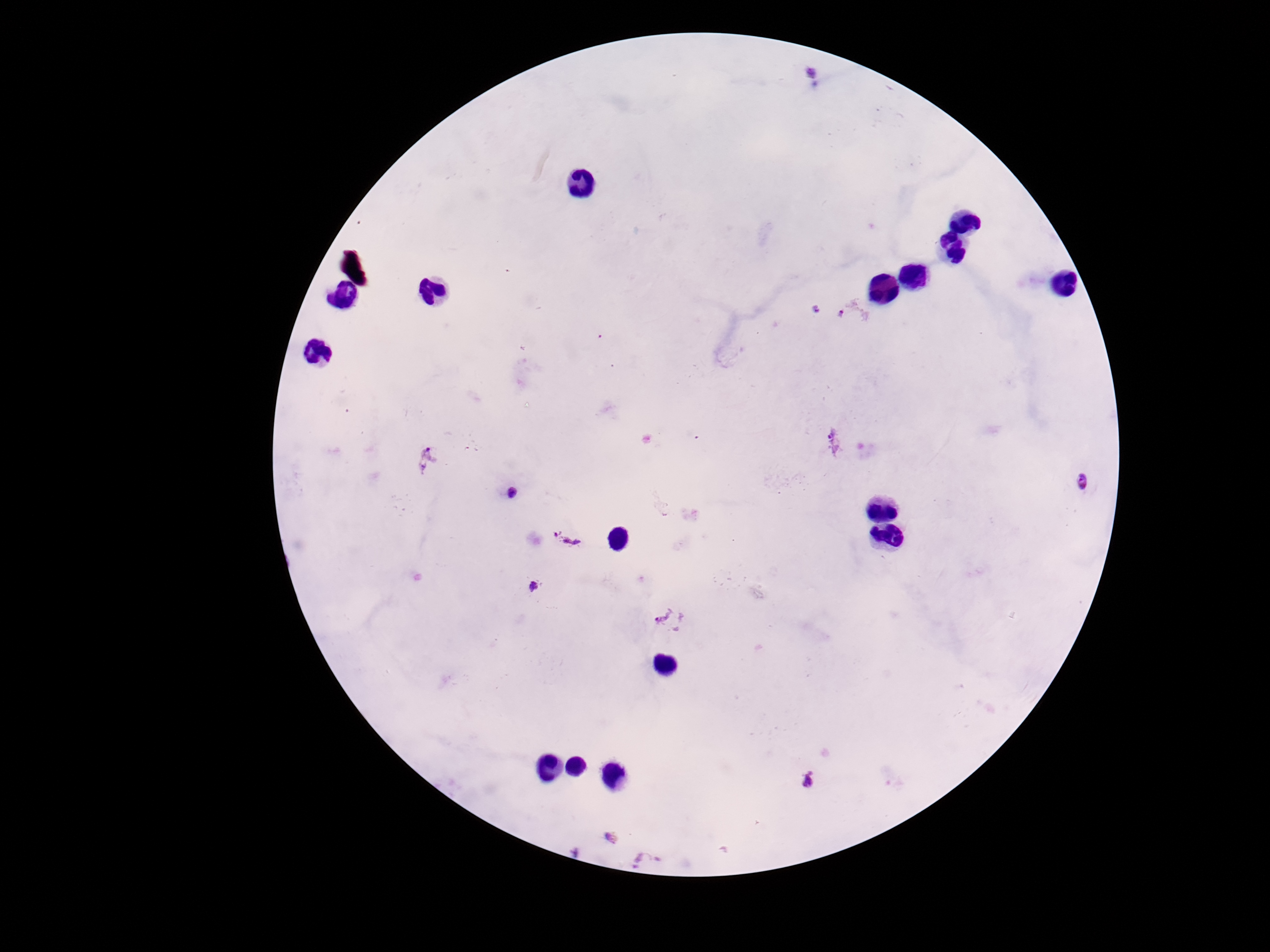
Approximate object centers, in pixels from the top-left corner. Plasmodium parasite locations: (x=814, y=76), (x=816, y=309), (x=854, y=312), (x=834, y=441), (x=428, y=459), (x=1085, y=481), (x=513, y=492), (x=561, y=539), (x=535, y=588), (x=673, y=621), (x=808, y=779), (x=609, y=837), (x=649, y=861). Image is 1270×952 pixels. 100x magnification. Smartphone photograph taken through the microscope eyepiece. Thick blood film. Patient malaria status: positive. Giemsa stain. One field from this slide.